Name the cell type shown.
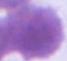

An erythrocyte.

Summary:
  - Magnification: 1000x
  - Modality: photomicrograph